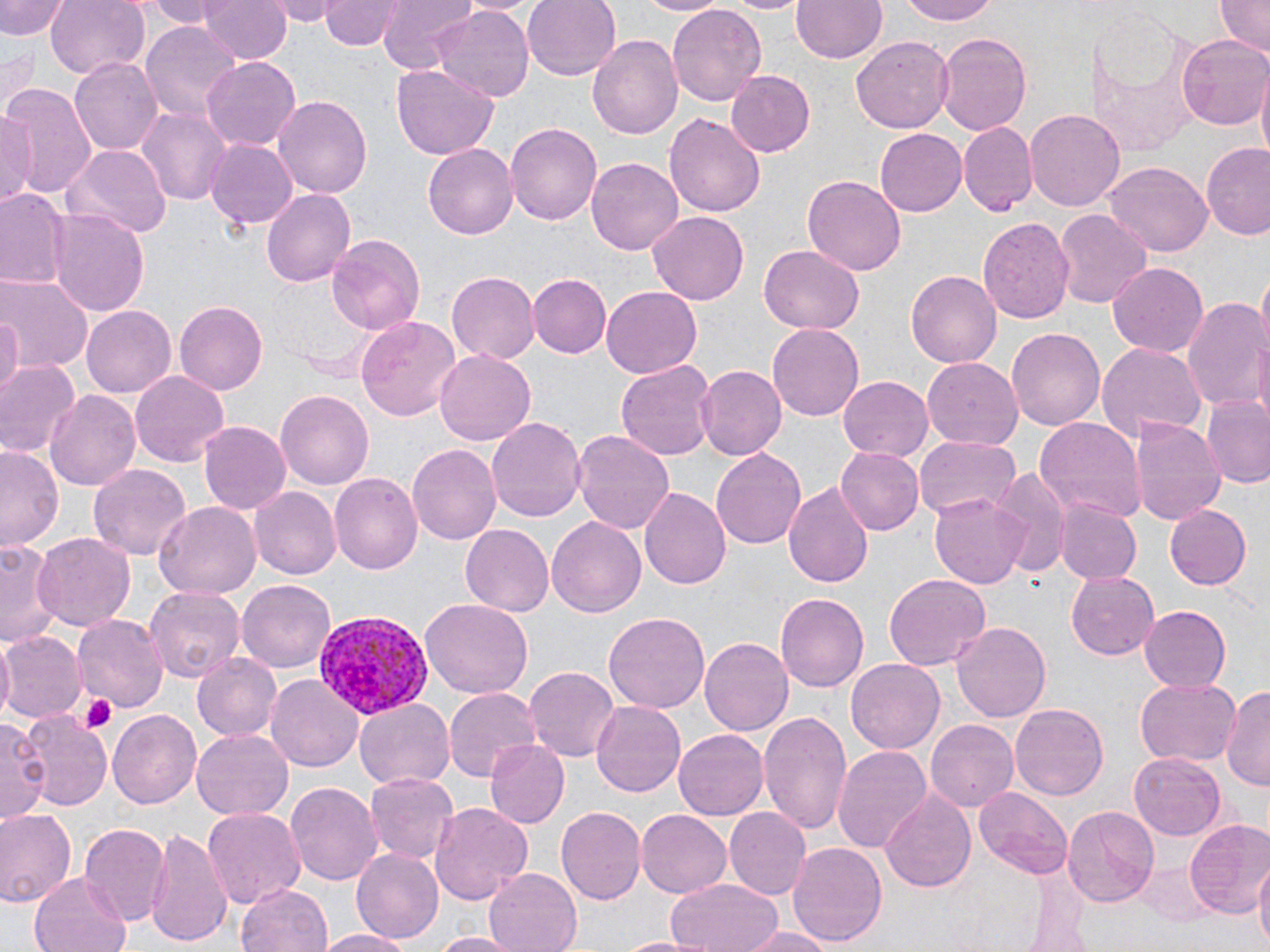

Summary:
  - Coordinate format: approximate bounding boxes as named x1/y1/x2/y2 corners in pixels
  - Uninfected red blood cell locations: (x1=0, y1=0, x2=69, y2=40), (x1=46, y1=0, x2=150, y2=79), (x1=137, y1=0, x2=227, y2=26), (x1=201, y1=0, x2=290, y2=64), (x1=266, y1=0, x2=342, y2=25), (x1=318, y1=0, x2=404, y2=50), (x1=377, y1=0, x2=480, y2=73), (x1=456, y1=0, x2=543, y2=19), (x1=522, y1=0, x2=623, y2=82), (x1=643, y1=0, x2=728, y2=16), (x1=724, y1=0, x2=809, y2=15), (x1=793, y1=0, x2=887, y2=64), (x1=894, y1=0, x2=1003, y2=26), (x1=1214, y1=0, x2=1268, y2=57), (x1=668, y1=2, x2=766, y2=106), (x1=1089, y1=2, x2=1201, y2=150), (x1=434, y1=6, x2=534, y2=104), (x1=139, y1=22, x2=245, y2=121), (x1=934, y1=32, x2=1033, y2=134), (x1=852, y1=33, x2=953, y2=132), (x1=1175, y1=34, x2=1270, y2=132), (x1=589, y1=35, x2=687, y2=140), (x1=1, y1=44, x2=38, y2=115), (x1=72, y1=56, x2=164, y2=157), (x1=201, y1=57, x2=302, y2=150), (x1=390, y1=66, x2=497, y2=157), (x1=725, y1=70, x2=815, y2=156), (x1=1256, y1=76, x2=1270, y2=168), (x1=0, y1=82, x2=98, y2=199), (x1=273, y1=95, x2=374, y2=196), (x1=137, y1=104, x2=231, y2=208), (x1=1024, y1=107, x2=1124, y2=209), (x1=0, y1=108, x2=37, y2=204), (x1=665, y1=112, x2=767, y2=217), (x1=504, y1=122, x2=602, y2=226), (x1=959, y1=122, x2=1038, y2=215), (x1=876, y1=130, x2=966, y2=214), (x1=204, y1=139, x2=298, y2=231), (x1=1200, y1=142, x2=1270, y2=238), (x1=67, y1=143, x2=170, y2=237), (x1=423, y1=143, x2=517, y2=239), (x1=587, y1=158, x2=682, y2=254), (x1=1106, y1=162, x2=1211, y2=256), (x1=803, y1=174, x2=906, y2=274), (x1=262, y1=184, x2=355, y2=284), (x1=0, y1=186, x2=67, y2=290), (x1=1053, y1=207, x2=1151, y2=308), (x1=50, y1=208, x2=150, y2=320), (x1=648, y1=209, x2=752, y2=304), (x1=976, y1=216, x2=1074, y2=324), (x1=324, y1=231, x2=427, y2=335), (x1=759, y1=246, x2=864, y2=334), (x1=1109, y1=261, x2=1211, y2=358), (x1=447, y1=271, x2=540, y2=364), (x1=906, y1=271, x2=1003, y2=367), (x1=527, y1=273, x2=611, y2=358), (x1=0, y1=276, x2=92, y2=373), (x1=602, y1=288, x2=702, y2=376), (x1=1181, y1=292, x2=1267, y2=413), (x1=173, y1=299, x2=269, y2=395), (x1=80, y1=304, x2=177, y2=397), (x1=0, y1=313, x2=22, y2=400), (x1=356, y1=315, x2=461, y2=422), (x1=767, y1=322, x2=864, y2=422), (x1=1006, y1=326, x2=1105, y2=433), (x1=1095, y1=344, x2=1205, y2=448), (x1=433, y1=346, x2=535, y2=443), (x1=924, y1=358, x2=1023, y2=448), (x1=615, y1=359, x2=716, y2=461), (x1=0, y1=361, x2=80, y2=458), (x1=696, y1=366, x2=786, y2=461), (x1=130, y1=371, x2=229, y2=465), (x1=839, y1=374, x2=934, y2=460), (x1=45, y1=390, x2=143, y2=494), (x1=276, y1=390, x2=373, y2=490), (x1=1202, y1=394, x2=1270, y2=487), (x1=486, y1=417, x2=585, y2=526), (x1=1035, y1=418, x2=1144, y2=525), (x1=1129, y1=418, x2=1226, y2=528), (x1=199, y1=422, x2=290, y2=516), (x1=570, y1=427, x2=675, y2=535), (x1=916, y1=433, x2=1023, y2=522), (x1=407, y1=443, x2=501, y2=543), (x1=0, y1=444, x2=65, y2=551), (x1=836, y1=446, x2=924, y2=536), (x1=709, y1=447, x2=806, y2=550), (x1=89, y1=463, x2=193, y2=560), (x1=988, y1=466, x2=1069, y2=573), (x1=329, y1=473, x2=422, y2=575), (x1=783, y1=480, x2=875, y2=592), (x1=640, y1=485, x2=730, y2=590), (x1=250, y1=486, x2=339, y2=579), (x1=931, y1=489, x2=1030, y2=587), (x1=1056, y1=500, x2=1141, y2=584), (x1=155, y1=502, x2=259, y2=598), (x1=1167, y1=504, x2=1253, y2=590), (x1=547, y1=515, x2=646, y2=619), (x1=458, y1=523, x2=554, y2=616), (x1=33, y1=532, x2=135, y2=633), (x1=0, y1=538, x2=62, y2=647), (x1=1066, y1=571, x2=1161, y2=661), (x1=884, y1=572, x2=991, y2=672), (x1=237, y1=578, x2=340, y2=672), (x1=143, y1=586, x2=244, y2=684), (x1=775, y1=592, x2=869, y2=693), (x1=419, y1=598, x2=534, y2=698), (x1=1138, y1=605, x2=1230, y2=692), (x1=604, y1=612, x2=710, y2=716), (x1=73, y1=614, x2=167, y2=714), (x1=953, y1=621, x2=1050, y2=722), (x1=0, y1=630, x2=86, y2=724), (x1=700, y1=635, x2=796, y2=737), (x1=191, y1=653, x2=283, y2=742), (x1=846, y1=658, x2=945, y2=756), (x1=524, y1=665, x2=620, y2=761), (x1=264, y1=673, x2=364, y2=773), (x1=1136, y1=676, x2=1241, y2=767), (x1=1224, y1=682, x2=1270, y2=794), (x1=443, y1=686, x2=544, y2=782), (x1=353, y1=698, x2=454, y2=791), (x1=591, y1=701, x2=685, y2=799), (x1=1010, y1=703, x2=1107, y2=801), (x1=14, y1=708, x2=113, y2=812), (x1=106, y1=709, x2=203, y2=810), (x1=758, y1=709, x2=853, y2=837), (x1=1, y1=717, x2=46, y2=826), (x1=926, y1=718, x2=1020, y2=812), (x1=674, y1=728, x2=768, y2=822), (x1=191, y1=729, x2=294, y2=820), (x1=486, y1=740, x2=569, y2=831), (x1=832, y1=743, x2=931, y2=852), (x1=1128, y1=752, x2=1227, y2=841), (x1=362, y1=771, x2=461, y2=865), (x1=286, y1=779, x2=382, y2=886), (x1=879, y1=785, x2=976, y2=895), (x1=973, y1=786, x2=1073, y2=878), (x1=430, y1=802, x2=532, y2=905), (x1=1061, y1=804, x2=1161, y2=906), (x1=200, y1=805, x2=305, y2=910), (x1=555, y1=805, x2=645, y2=906), (x1=724, y1=807, x2=812, y2=901), (x1=0, y1=808, x2=77, y2=908), (x1=636, y1=810, x2=731, y2=897), (x1=1185, y1=819, x2=1270, y2=922), (x1=79, y1=824, x2=168, y2=925), (x1=143, y1=826, x2=234, y2=949), (x1=787, y1=840, x2=887, y2=947), (x1=353, y1=847, x2=444, y2=943), (x1=1254, y1=862, x2=1270, y2=952), (x1=484, y1=868, x2=583, y2=952), (x1=28, y1=874, x2=131, y2=952), (x1=663, y1=877, x2=782, y2=952), (x1=236, y1=881, x2=332, y2=952), (x1=738, y1=926, x2=837, y2=952), (x1=316, y1=928, x2=415, y2=952), (x1=432, y1=932, x2=522, y2=952), (x1=617, y1=936, x2=708, y2=952)
  - Plasmodium vivax-infected red blood cell locations: (x1=314, y1=612, x2=432, y2=718)
  - Platelet locations: (x1=81, y1=695, x2=118, y2=734)
  - Slide-level diagnosis: Plasmodium vivax
  - Magnification: 1000x
  - Image size: 1270×952 pixels
  - Stain: May-Grünwald-Giemsa
  - Field of view: one of a larger specimen
  - Preparation: thin blood smear
  - Modality: optical microscopy